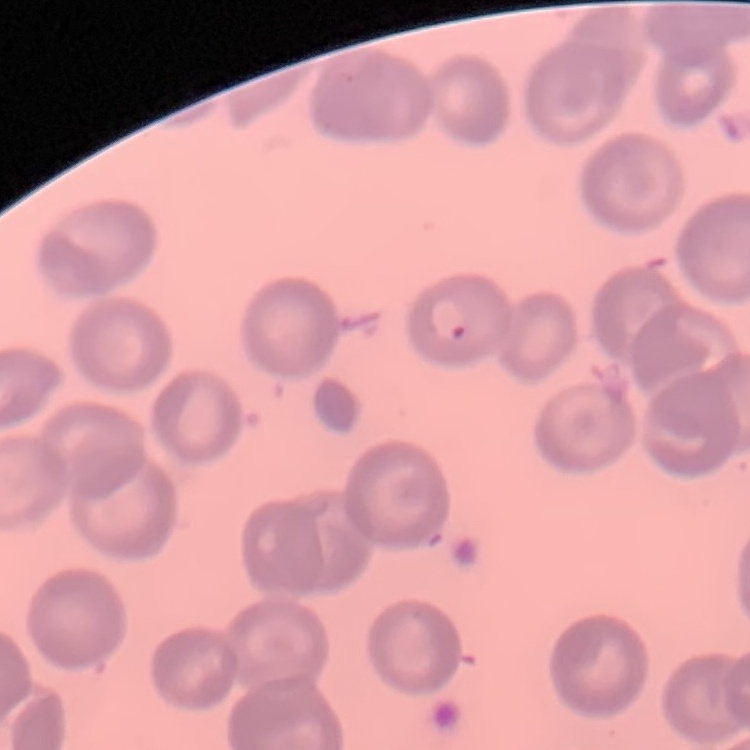

Summary:
  - Red blood cell morphology: no rouleaux formation
  - Preparation: thin blood smear
  - Image type: one tile cut from a larger photomicrograph
  - Stain: Field's or Giemsa